Classify this cell by malaria status.
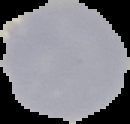
Uninfected.

The area outside the segmented cell region is set to black. Image is 130×124 pixels. From a thin blood smear.